Outline each uninfected red blood cell.
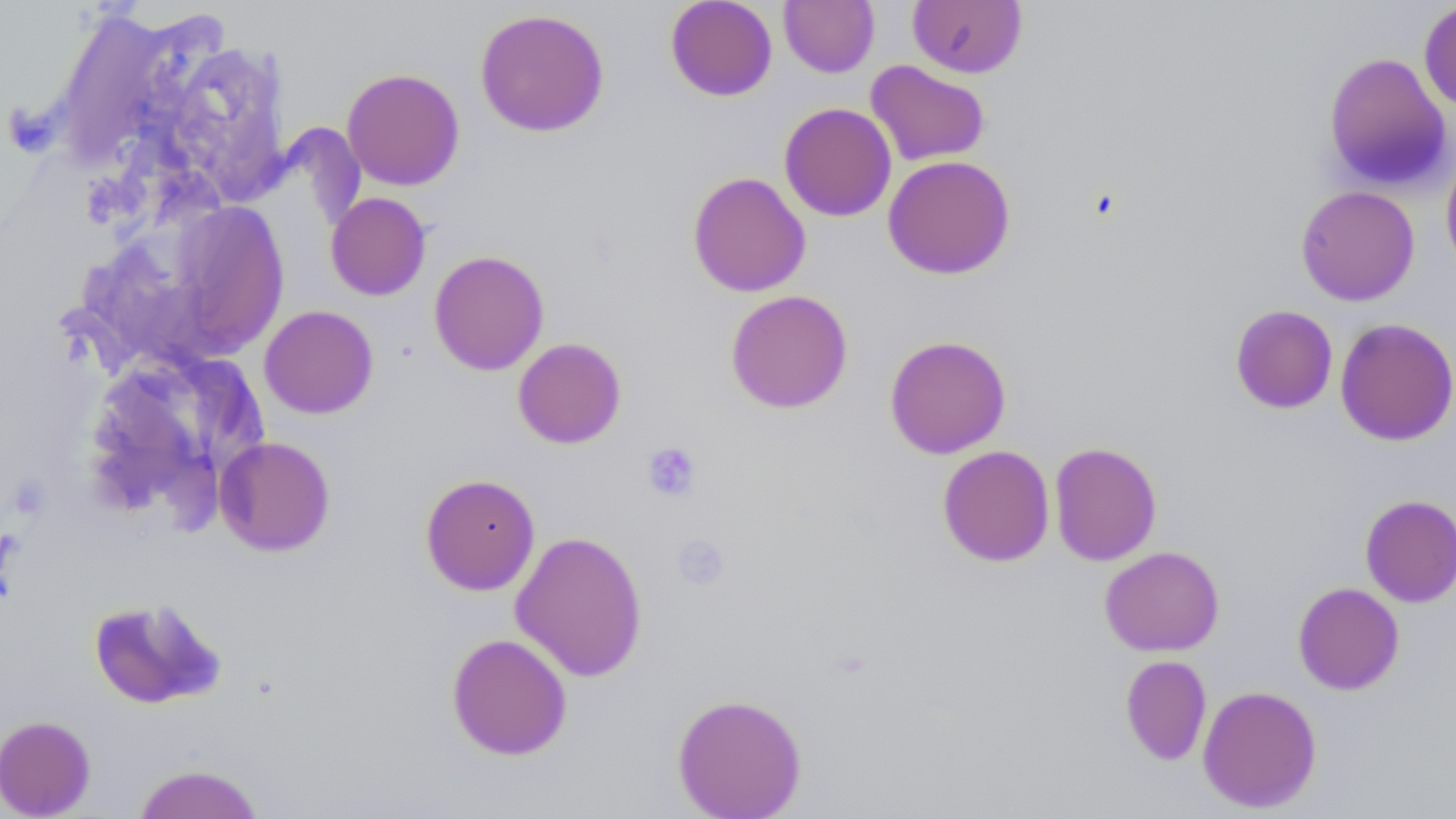
Approximate bounding boxes as (x1,y1)-(x2,y2) corner pairs in pixels.
Uninfected red blood cells: (665,0)-(777,101), (779,0)-(879,77), (907,0)-(1027,78), (1418,1)-(1456,112), (47,6)-(178,168), (474,8)-(610,137), (1322,50)-(1453,193), (865,60)-(990,167), (341,67)-(465,190), (778,102)-(897,222), (1440,149)-(1456,277), (882,154)-(1016,280), (687,171)-(811,297), (1295,185)-(1420,306), (325,192)-(431,301), (167,200)-(290,358), (428,250)-(549,376), (725,290)-(854,414), (1230,304)-(1338,414), (259,305)-(379,419), (1335,317)-(1456,446), (884,334)-(1011,459), (512,337)-(627,449), (79,351)-(264,528), (215,436)-(336,556), (1048,441)-(1162,566), (937,445)-(1055,567), (420,473)-(541,595), (1360,494)-(1456,607), (510,530)-(649,682), (1099,546)-(1224,656), (1292,582)-(1405,695), (87,597)-(226,710), (446,632)-(573,761), (1119,655)-(1212,766), (1197,684)-(1322,813), (671,693)-(807,818), (0,715)-(96,818), (133,763)-(265,819).

Platelet locations: (642,441)-(702,502), (672,533)-(731,590). Slide-level diagnosis: negative for blood parasites. Image is 1456×819 pixels. Thin blood film. 1000x magnification. Single field of view. Optical microscopy. May-Grünwald-Giemsa-stained preparation.